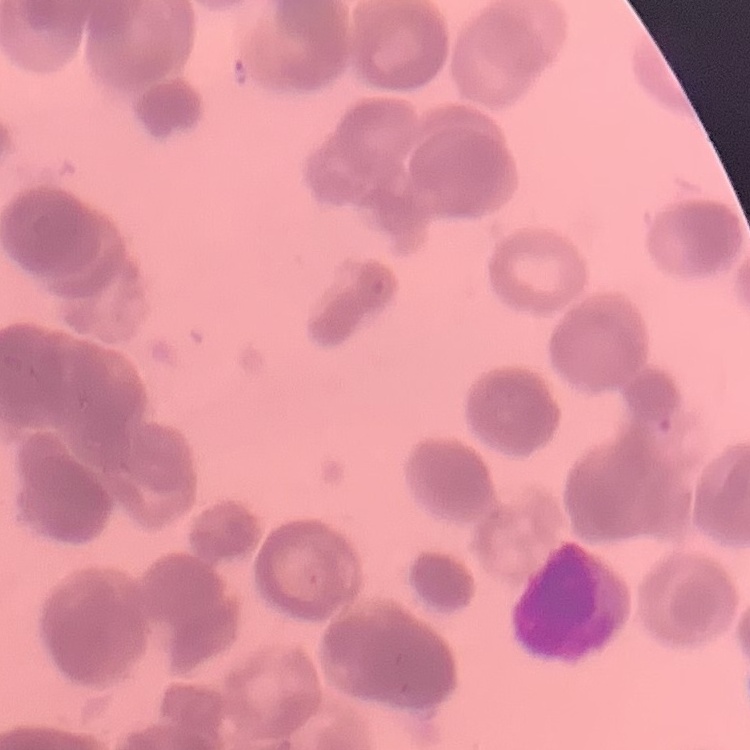 The erythrocytes show rouleaux formation. Thin blood film. Square crop of a larger photomicrograph. Stained with either Field's or Giemsa.